Evaluate for malaria.
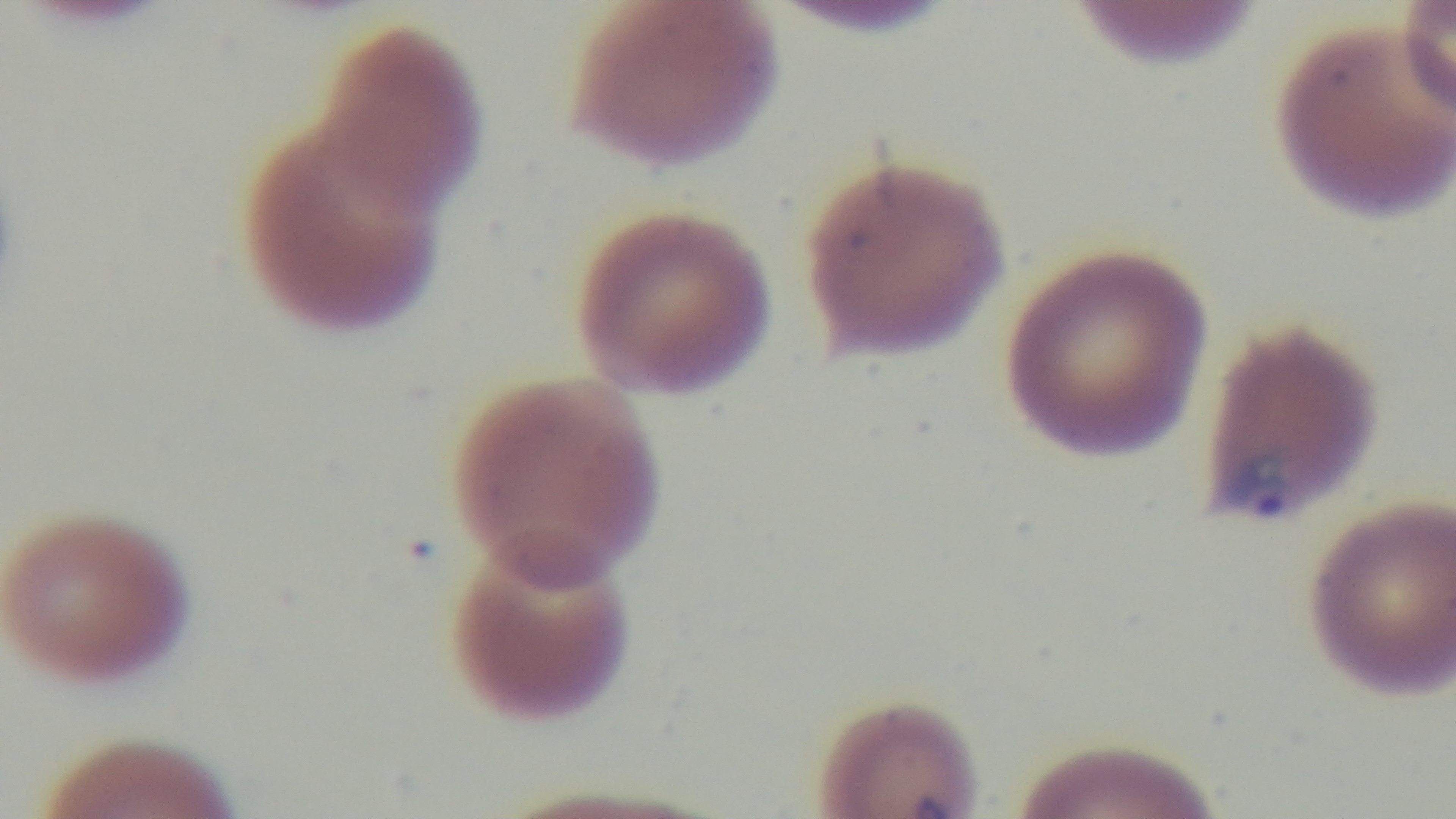
Infected.

{
  "objective": "100x oil immersion",
  "preparation": "thin smear",
  "field_of_view": "single",
  "stain": "Giemsa",
  "capture": "mounted 4K digital camera",
  "modality": "light microscopy"
}